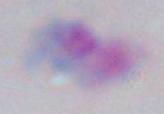
Summary:
  - Modality: micrograph
  - Magnification: 1000x
  - Identification: Toxoplasma gondii